Mark where platelets are.
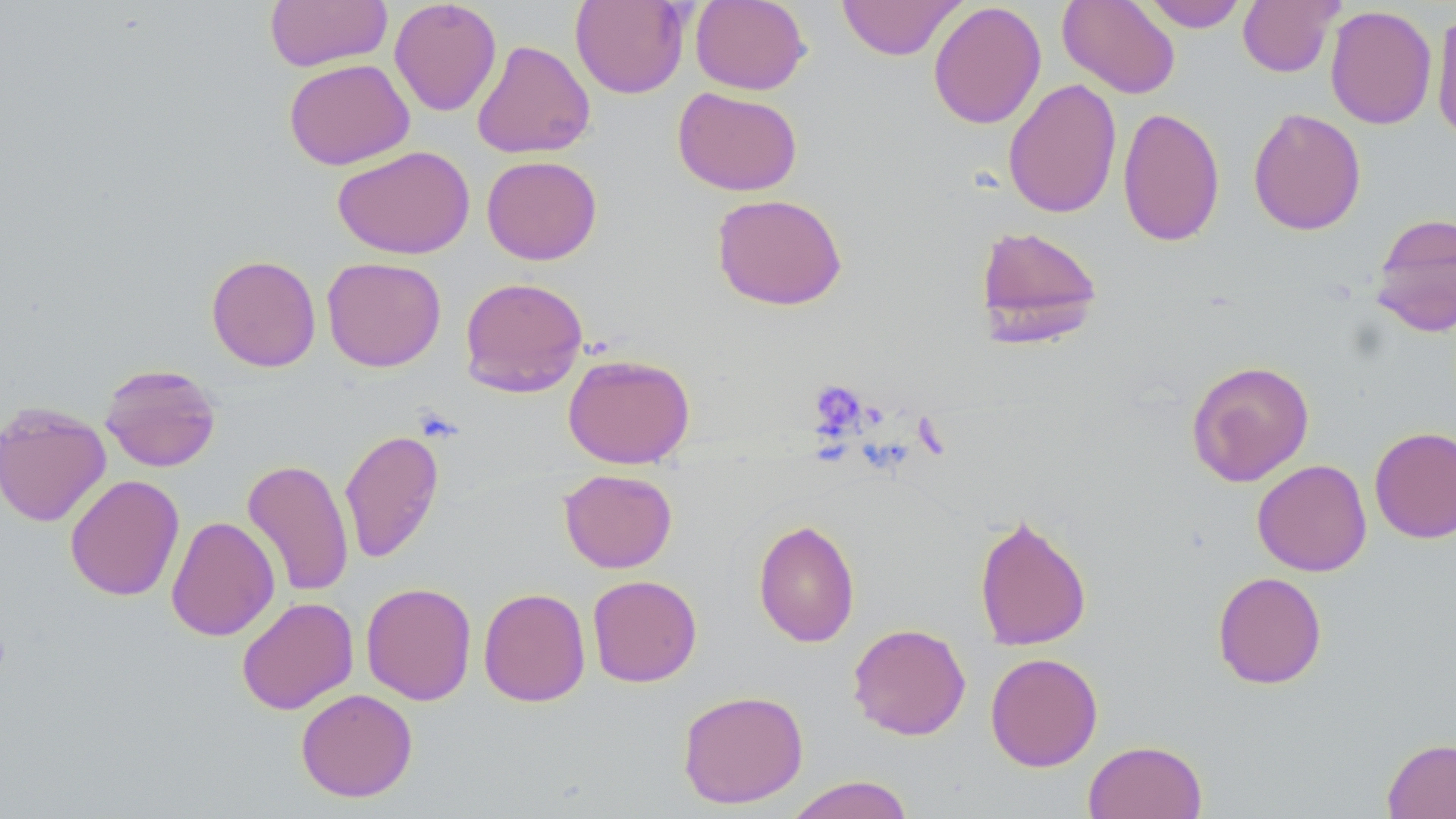

Approximate bounding boxes as (x1, y1, x2, y2) in pixels.
Platelets: (810, 380, 867, 436).

Summary:
  - Uninfected red blood cell locations: (265, 0, 392, 72), (389, 0, 502, 116), (570, 0, 690, 99), (690, 0, 810, 95), (837, 0, 965, 61), (1057, 0, 1181, 99), (1142, 0, 1249, 32), (1238, 0, 1342, 77), (928, 1, 1046, 130), (1325, 5, 1437, 130), (1430, 11, 1456, 145), (471, 39, 595, 160), (283, 58, 415, 170), (1003, 78, 1123, 218), (672, 87, 803, 196), (1117, 106, 1225, 247), (1247, 107, 1367, 236), (333, 145, 475, 259), (481, 155, 602, 265), (711, 193, 848, 310), (1370, 211, 1456, 338), (973, 224, 1104, 347), (206, 254, 321, 372), (322, 256, 446, 372), (459, 276, 589, 397), (563, 353, 695, 469), (1186, 359, 1315, 487), (99, 363, 221, 472), (0, 401, 111, 527), (1369, 426, 1456, 543), (339, 428, 445, 564), (242, 458, 354, 598), (1252, 459, 1372, 577), (559, 468, 678, 573), (64, 474, 184, 601), (973, 512, 1092, 652), (166, 515, 280, 641), (753, 518, 860, 648), (1212, 571, 1327, 689), (587, 574, 702, 687), (360, 582, 477, 705), (478, 587, 591, 707), (236, 596, 359, 715), (848, 623, 971, 741), (985, 652, 1103, 771), (295, 688, 418, 802), (677, 689, 809, 808), (1382, 737, 1456, 819), (1083, 739, 1208, 819), (784, 775, 915, 819)
  - Slide-level diagnosis: no evidence of blood parasites
  - Magnification: 1000x
  - Image size: 1456×819 pixels
  - Stain: May-Grünwald-Giemsa
  - Field of view: one of a larger specimen
  - Preparation: thin blood film
  - Modality: light microscopy